Give the extent of all uninfected red blood cells.
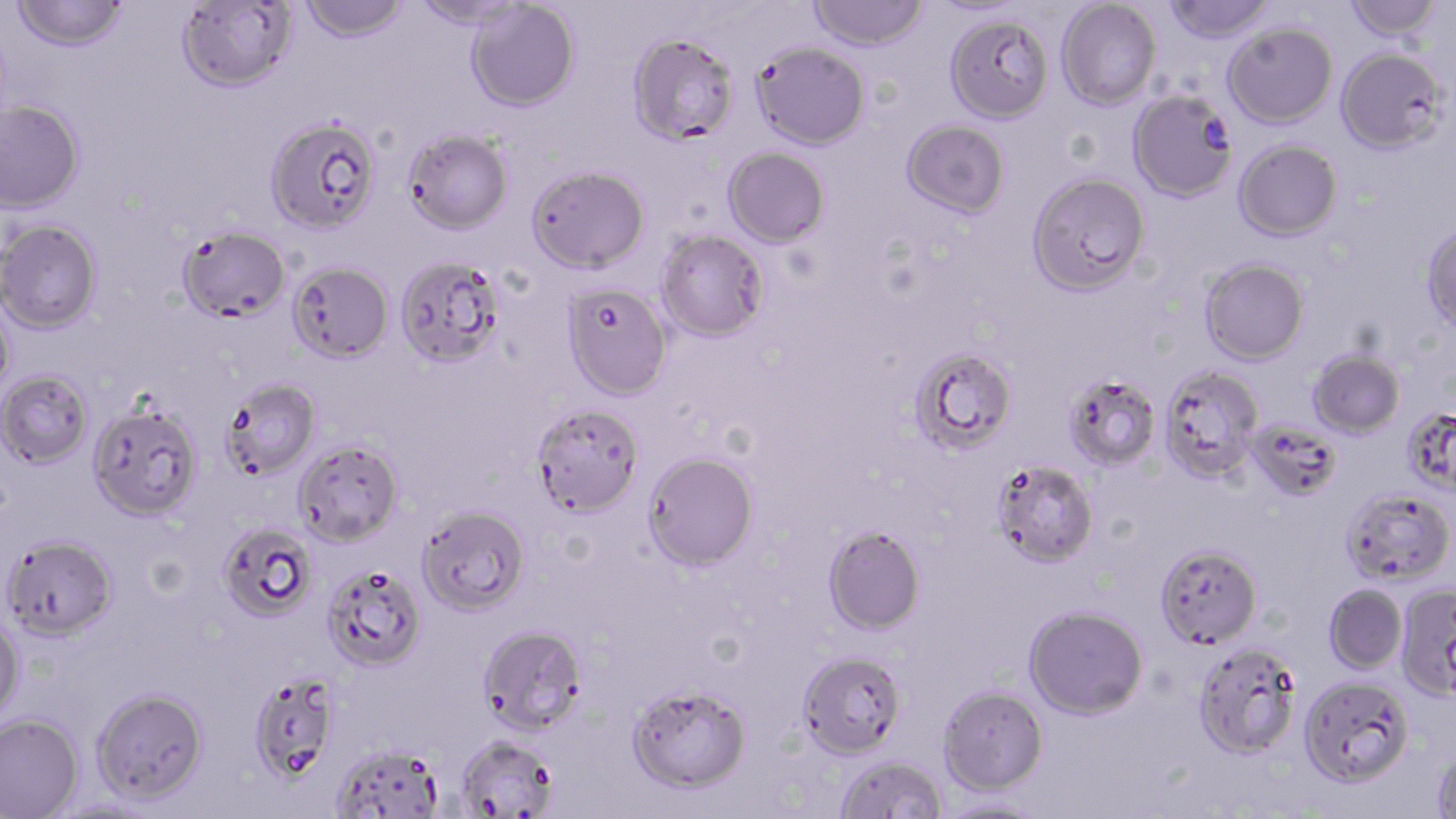
Approximate bounding boxes as (x1,y1)-(x2,y2) corner pairs in pixels.
Uninfected red blood cells: (11,0)-(129,52), (300,0)-(409,43), (410,0)-(531,30), (808,0)-(930,52), (1162,0)-(1276,44), (1344,0)-(1444,42), (175,1)-(298,92), (466,1)-(580,112), (1057,1)-(1161,109), (944,13)-(1053,124), (1223,22)-(1338,128), (626,32)-(739,146), (751,41)-(870,150), (1335,47)-(1449,155), (1128,91)-(1238,203), (0,98)-(84,213), (265,116)-(382,235), (900,120)-(1010,220), (403,128)-(514,234), (1233,140)-(1342,241), (722,148)-(830,249), (526,164)-(650,274), (1027,173)-(1151,298), (0,219)-(102,333), (1421,223)-(1456,335), (177,226)-(291,323), (656,232)-(771,345), (396,257)-(507,370), (1200,258)-(1309,366), (286,261)-(394,364), (563,285)-(673,402), (0,295)-(16,403), (909,348)-(1019,457), (1308,349)-(1405,438), (1159,366)-(1264,483), (0,370)-(93,468), (1063,377)-(1162,472), (221,379)-(321,480), (87,402)-(203,521), (532,405)-(644,521), (1402,407)-(1456,497), (1246,422)-(1343,503), (293,439)-(403,547), (643,453)-(760,573), (991,461)-(1098,570), (1341,487)-(1455,585), (416,505)-(531,616), (216,522)-(317,621), (823,526)-(926,636), (1,533)-(118,641), (1155,543)-(1263,649), (321,563)-(426,671), (1395,583)-(1456,699), (1323,584)-(1407,674), (1023,606)-(1148,720), (0,616)-(25,723), (478,624)-(588,735), (1193,643)-(1302,759), (797,651)-(907,762), (248,672)-(340,786), (1299,675)-(1414,788), (627,686)-(751,795), (938,686)-(1048,797), (90,687)-(208,806), (0,713)-(83,818), (456,735)-(558,818), (330,744)-(444,817), (1431,749)-(1456,817), (835,756)-(948,818), (936,798)-(1045,819).

Summary:
  - Slide-level diagnosis: Plasmodium falciparum
  - Field of view: single
  - Preparation: thin blood smear
  - Modality: light microscopy
  - Stain: May-Grünwald-Giemsa
  - Image size: 1456×819 pixels
  - Magnification: 1000x